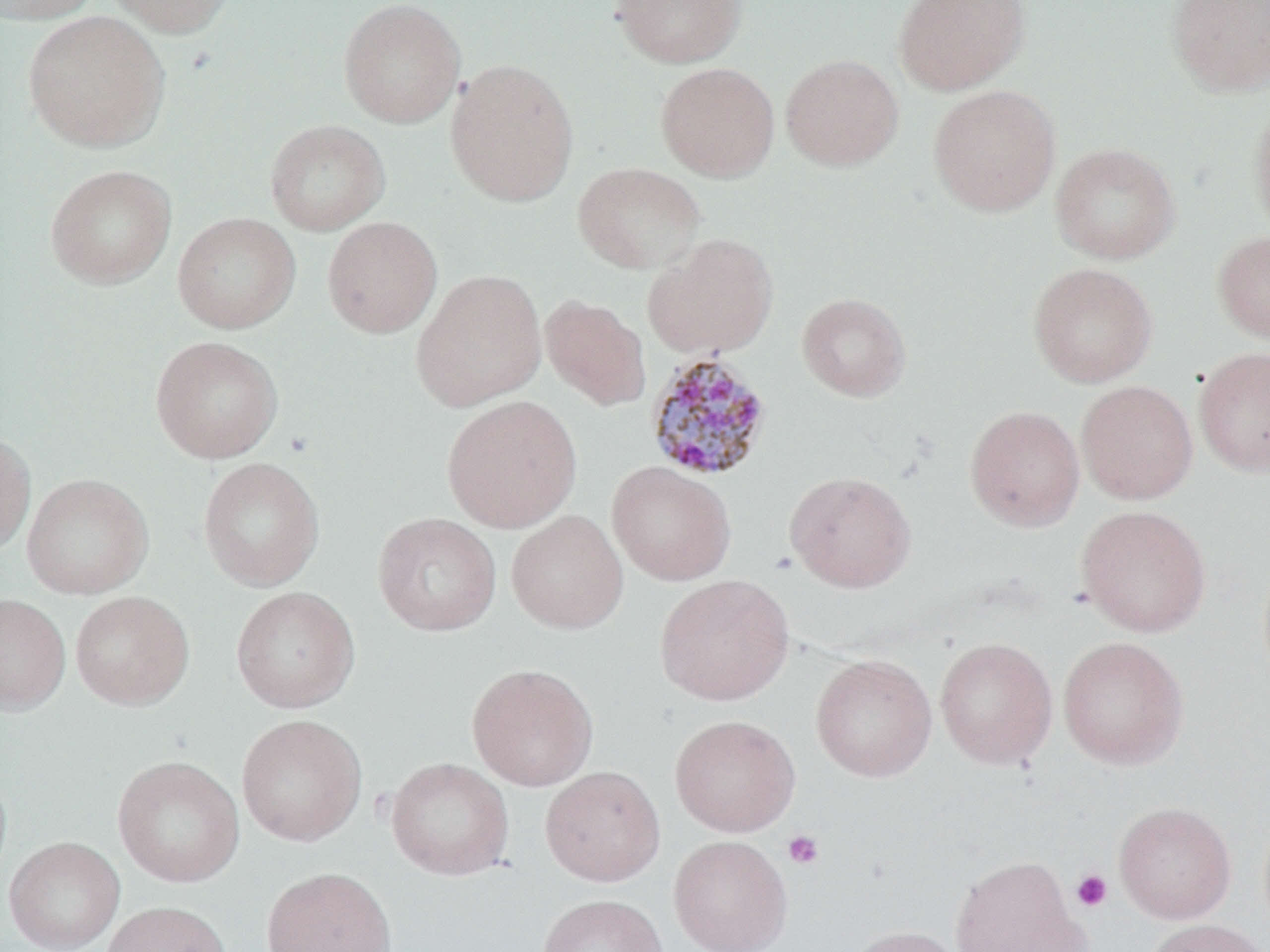

Approximate bounding boxes as (x1, y1, x2, y2) in pixels. Uninfected red blood cell locations: (1, 0, 102, 25), (104, 0, 238, 38), (610, 0, 747, 68), (892, 0, 1031, 96), (1165, 0, 1270, 98), (338, 1, 465, 129), (22, 11, 171, 153), (780, 53, 904, 171), (445, 58, 579, 207), (656, 62, 780, 182), (928, 84, 1062, 217), (1249, 101, 1270, 241), (264, 119, 391, 236), (1050, 142, 1181, 265), (572, 162, 706, 274), (44, 164, 177, 289), (172, 212, 301, 334), (322, 216, 442, 338), (1212, 230, 1270, 344), (644, 233, 778, 360), (1027, 262, 1158, 388), (411, 269, 547, 411), (796, 292, 911, 402), (540, 295, 651, 411), (150, 336, 284, 463), (1193, 346, 1270, 477), (1076, 380, 1198, 505), (441, 394, 582, 533), (964, 405, 1085, 532), (0, 430, 36, 558), (198, 457, 325, 591), (606, 461, 737, 586), (784, 470, 917, 593), (22, 472, 154, 599), (1076, 505, 1211, 637), (506, 510, 629, 634), (372, 512, 502, 636), (655, 574, 795, 706), (230, 585, 360, 713), (69, 591, 195, 710), (0, 593, 71, 715), (1057, 636, 1189, 770), (934, 637, 1058, 769), (810, 653, 937, 782), (466, 662, 599, 791), (235, 714, 367, 847), (669, 714, 800, 836), (112, 754, 245, 888), (385, 757, 515, 880), (0, 765, 13, 894), (540, 765, 666, 886), (1113, 801, 1236, 923), (668, 835, 793, 952), (3, 836, 125, 952), (948, 854, 1086, 952), (261, 866, 397, 952), (537, 893, 667, 952), (100, 900, 232, 952), (1144, 918, 1268, 952), (846, 924, 968, 952). Plasmodium malariae-infected red blood cell locations: (644, 351, 775, 482). Platelet locations: (782, 829, 824, 870), (1071, 869, 1112, 911). Slide-level diagnosis: Plasmodium malariae. May-Grünwald-Giemsa stain. Thin blood film. Optical microscopy. One field of a larger specimen. Captured at 1000x magnification. Image is 1270×952 pixels.